Report the malaria status of this cell.
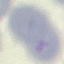
It is uninfected.

Giemsa-stained preparation. Acquired by smartphone through the microscope eyepiece. Automatically extracted cell patch, resized to 64 × 64 pixels. Thin blood film.